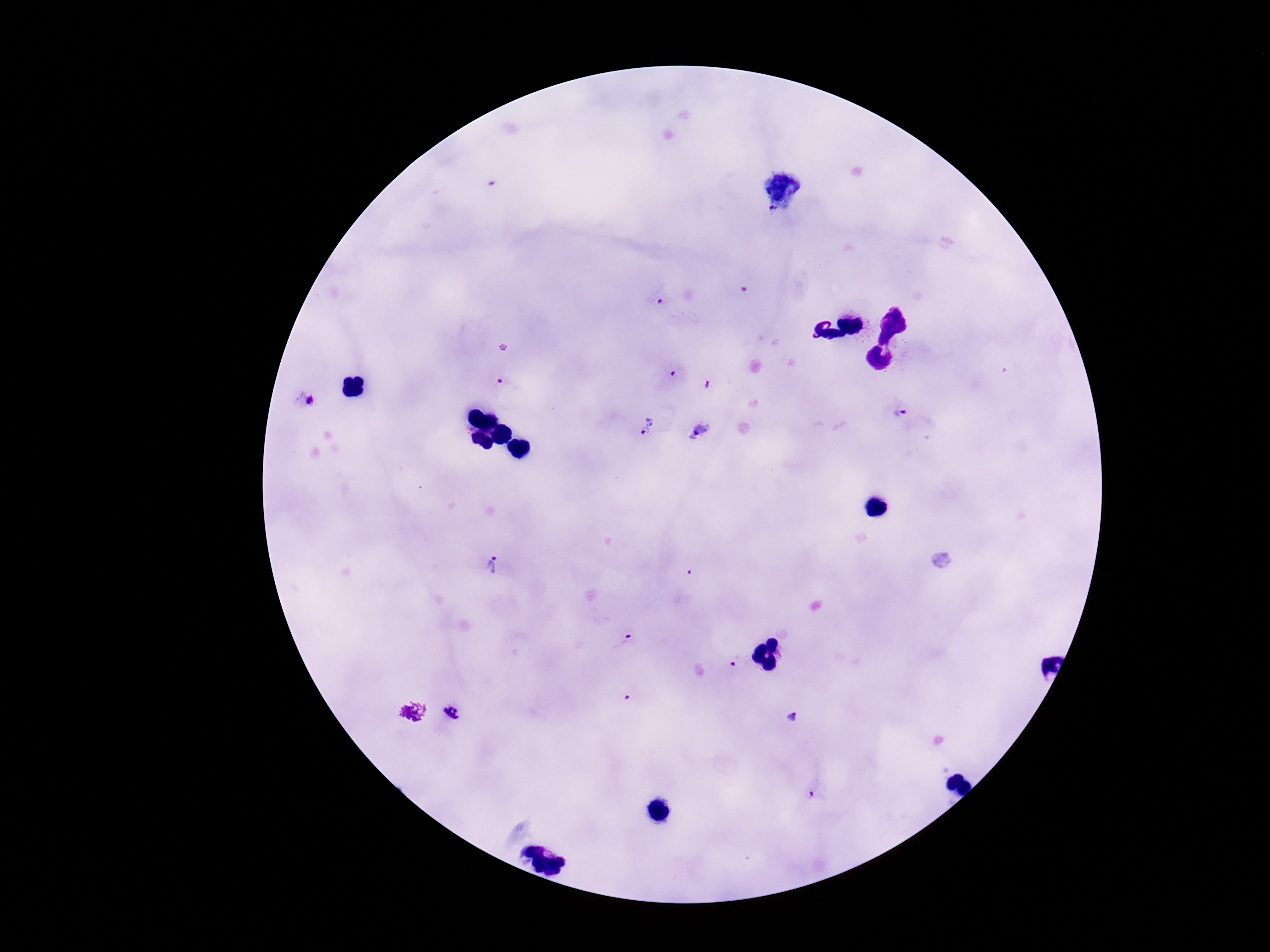

Approximate object centers, in pixels from the top-left corner.
Summary:
  - Plasmodium parasite locations: (x=771, y=214), (x=659, y=302), (x=672, y=377), (x=500, y=382), (x=309, y=400), (x=901, y=414), (x=651, y=417), (x=701, y=433), (x=642, y=434), (x=488, y=564), (x=624, y=641), (x=731, y=667), (x=627, y=697), (x=452, y=713), (x=793, y=718), (x=811, y=795)
  - Image size: 1270×952 pixels
  - Field of view: one from this slide
  - Magnification: 100x
  - Stain: Giemsa
  - Preparation: thick blood film
  - Patient malaria status: positive
  - Capture: smartphone camera through the microscope eyepiece